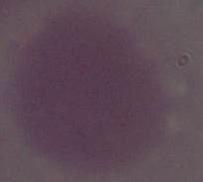
Summary:
  - Magnification: 1000x
  - Modality: photomicrograph
  - Identification: erythrocyte